Point out each malaria parasite and each leukocyte.
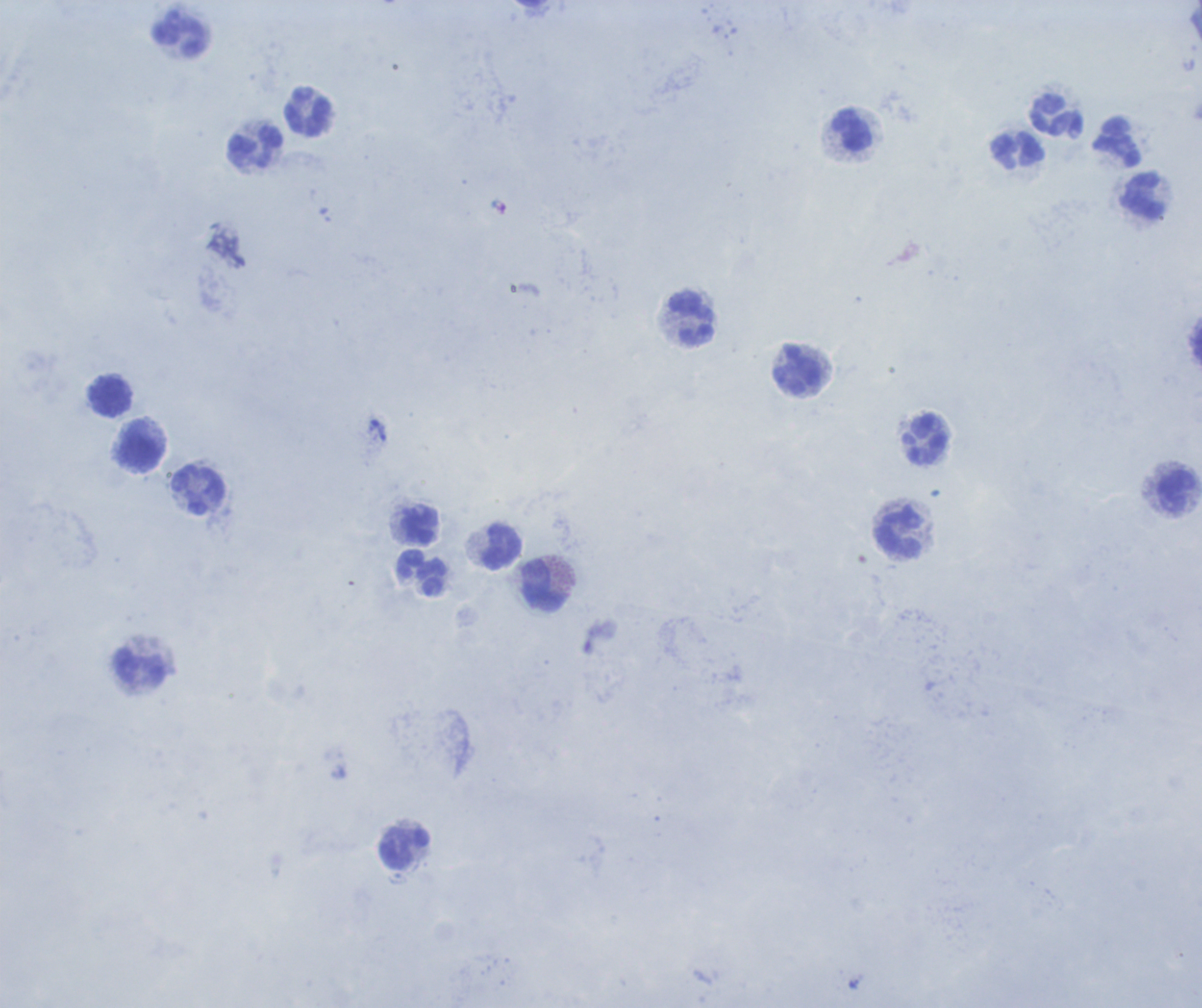

No malaria parasites detected.
Approximate centers as [x, y] in pixels.
Leukocytes: [181, 38], [308, 112], [1057, 117], [853, 131], [1118, 144], [256, 149], [1017, 150], [1143, 197], [691, 319], [799, 372], [111, 396], [926, 440], [139, 453], [200, 492], [1178, 494], [421, 525], [899, 533], [501, 548], [423, 574], [541, 587], [141, 668], [404, 848].

Thick blood smear. Background quality: poor. Captured at 100x magnification. Single field of view. Image is 1202×1008 pixels. Previously used in an actual diagnosis. Romanowsky-stained preparation.